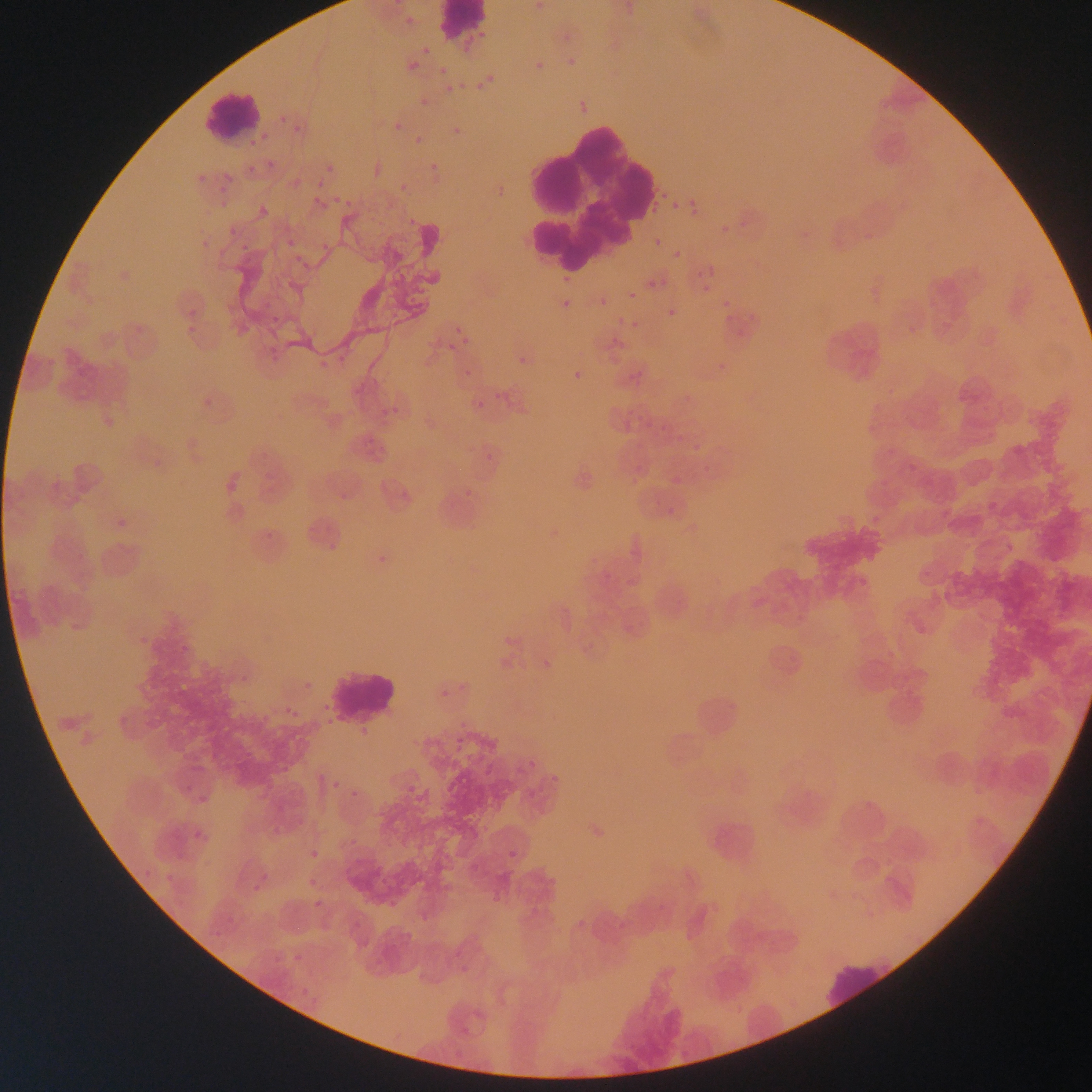
Approximate bounding boxes as [left, top, right, bottom] in pixels.
Summary:
  - Leukocyte locations: [435, 0, 488, 43], [202, 88, 260, 141], [511, 107, 663, 279], [329, 664, 397, 725], [684, 682, 747, 748], [706, 811, 769, 872], [819, 954, 895, 1012]
  - Plasmodium parasite locations: [531, 0, 548, 17], [401, 11, 421, 31], [557, 27, 576, 47], [418, 43, 434, 59], [562, 54, 581, 72], [531, 57, 549, 77], [405, 58, 422, 75], [435, 63, 451, 78], [478, 69, 500, 89], [442, 81, 458, 96], [417, 95, 432, 110], [276, 112, 290, 126], [282, 114, 305, 134], [392, 120, 405, 134], [290, 121, 306, 137], [448, 122, 466, 140], [412, 134, 427, 148], [264, 158, 279, 173], [426, 161, 443, 179], [244, 163, 259, 177], [325, 163, 338, 176], [195, 168, 207, 187], [219, 170, 235, 187], [312, 178, 331, 193], [391, 183, 412, 191], [333, 190, 340, 205], [311, 194, 326, 209], [342, 197, 355, 211], [217, 198, 231, 210], [256, 199, 273, 215], [686, 199, 704, 219], [669, 201, 682, 214], [716, 218, 735, 238], [226, 224, 240, 239], [862, 230, 873, 241], [285, 235, 301, 249], [651, 236, 663, 250], [317, 239, 332, 253], [238, 241, 254, 257], [670, 248, 683, 261], [286, 256, 299, 264], [297, 260, 308, 270], [700, 263, 719, 280], [643, 275, 659, 291], [699, 282, 713, 296], [627, 290, 639, 301], [259, 292, 273, 310], [596, 294, 610, 308], [557, 295, 576, 316], [719, 302, 740, 331], [184, 303, 200, 319], [665, 306, 679, 321], [748, 310, 758, 326], [267, 312, 280, 325], [629, 318, 643, 333], [184, 323, 196, 334], [450, 324, 472, 350], [608, 333, 624, 349], [264, 343, 279, 357], [335, 345, 349, 363], [514, 352, 534, 372], [715, 358, 728, 374], [568, 366, 588, 386], [460, 370, 469, 378], [626, 371, 649, 383], [493, 386, 504, 405], [681, 392, 697, 403], [469, 394, 489, 413], [198, 397, 213, 409], [385, 403, 404, 422], [624, 407, 633, 415], [643, 417, 656, 428], [671, 427, 695, 442], [693, 442, 701, 456], [368, 444, 381, 458], [481, 454, 493, 462], [700, 465, 711, 474], [262, 469, 272, 480], [879, 476, 893, 490], [459, 480, 479, 499], [628, 481, 639, 490], [396, 484, 411, 500], [334, 488, 349, 505], [666, 496, 682, 517], [117, 515, 128, 526], [302, 525, 313, 534], [259, 528, 275, 540], [327, 542, 340, 553], [372, 550, 394, 575], [853, 572, 865, 585], [497, 633, 517, 646], [134, 640, 148, 647], [175, 642, 186, 655], [542, 659, 554, 669], [235, 662, 256, 684], [301, 678, 311, 689], [436, 690, 454, 701], [318, 703, 330, 717], [288, 707, 303, 720], [357, 727, 368, 738], [449, 733, 459, 743], [188, 761, 206, 772], [524, 761, 536, 772], [277, 766, 286, 775], [543, 773, 560, 780], [329, 778, 342, 792], [179, 784, 191, 793], [406, 785, 416, 794], [349, 788, 362, 801], [190, 791, 211, 807], [864, 800, 880, 812], [269, 818, 283, 838], [192, 831, 198, 840], [349, 836, 357, 847], [202, 838, 211, 846], [504, 846, 523, 865], [308, 848, 321, 861], [139, 865, 155, 882], [257, 872, 273, 881], [370, 872, 388, 888], [161, 873, 181, 883], [304, 878, 312, 889], [248, 885, 256, 893], [310, 899, 323, 915], [224, 914, 238, 928], [569, 918, 585, 926], [208, 927, 223, 938], [291, 951, 304, 963], [269, 957, 280, 971], [456, 965, 470, 978], [298, 985, 311, 1001]
  - Image size: 1092×1092 pixels
  - Capture: mobile-phone photograph through a microscope
  - Preparation: thin blood film
  - Field of view: single
  - Country: Ghana